Point out each leukocyte.
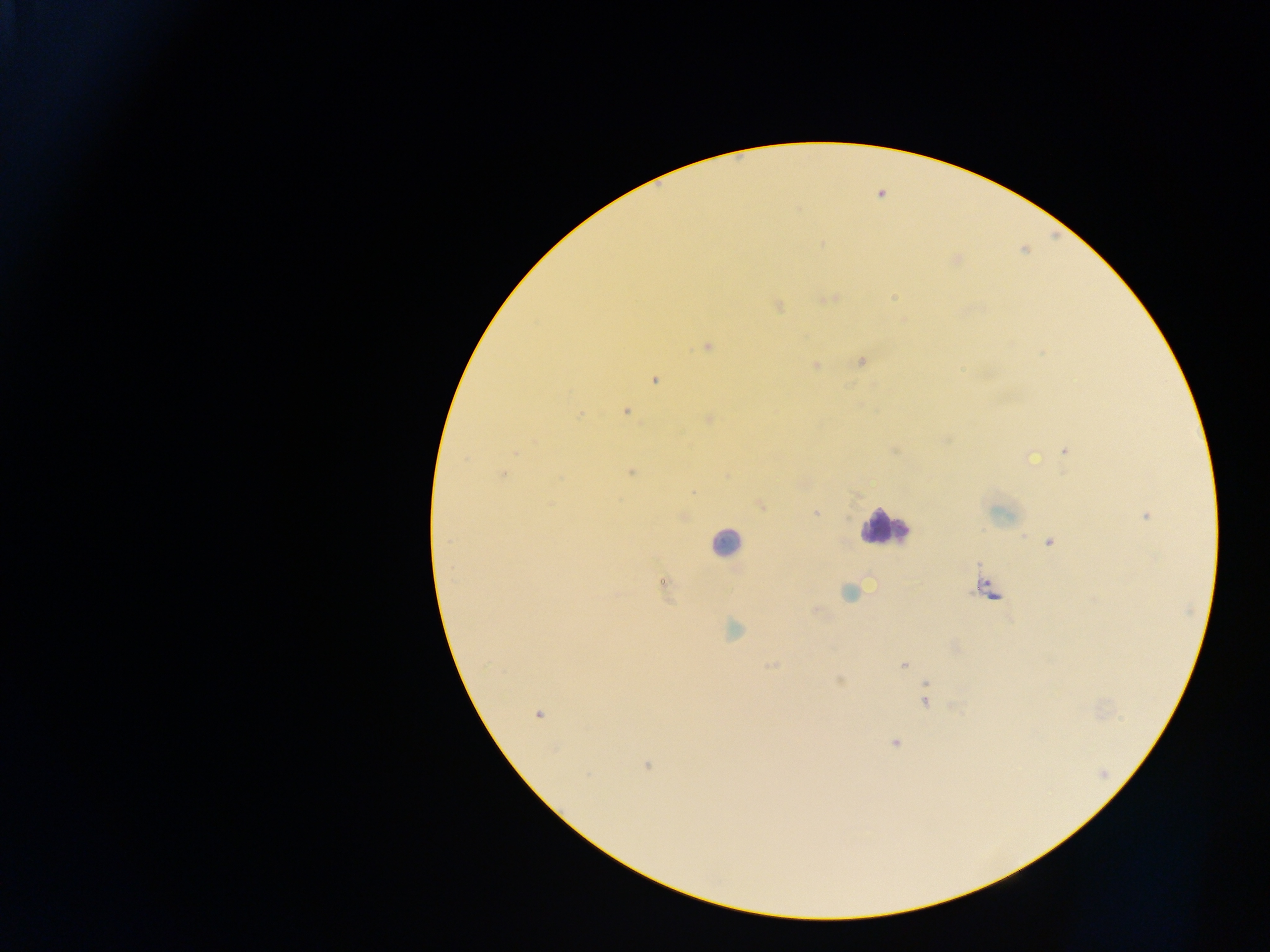
Approximate centers as x y in pixels.
Leukocytes: 884 528; 726 544; 989 589.

Summary:
  - Plasmodium parasite locations: 881 194; 892 297; 828 298; 778 305; 707 346; 861 361; 816 365; 655 380; 626 411; 579 414; 709 419; 945 439; 1064 450; 1030 456; 630 471; 501 474; 693 491; 760 504; 815 513; 1145 515; 682 516; 1050 541; 662 582; 849 592; 815 611; 732 629; 904 664; 770 665; 839 679; 925 684; 924 700; 537 714; 894 742; 646 765
  - Field of view: single
  - Country: Ghana
  - Preparation: thick blood film
  - Image size: 1270×952 pixels
  - Capture: mobile-phone photograph through a microscope